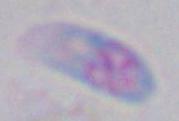

{
  "modality": "micrograph",
  "magnification": "1000x",
  "identification": "Toxoplasma gondii"
}